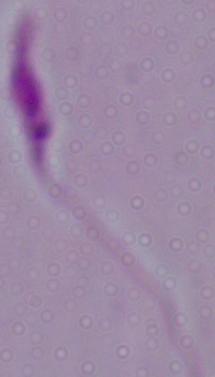
Summary:
  - Identification: Leishmania
  - Modality: photomicrograph
  - Magnification: 1000x